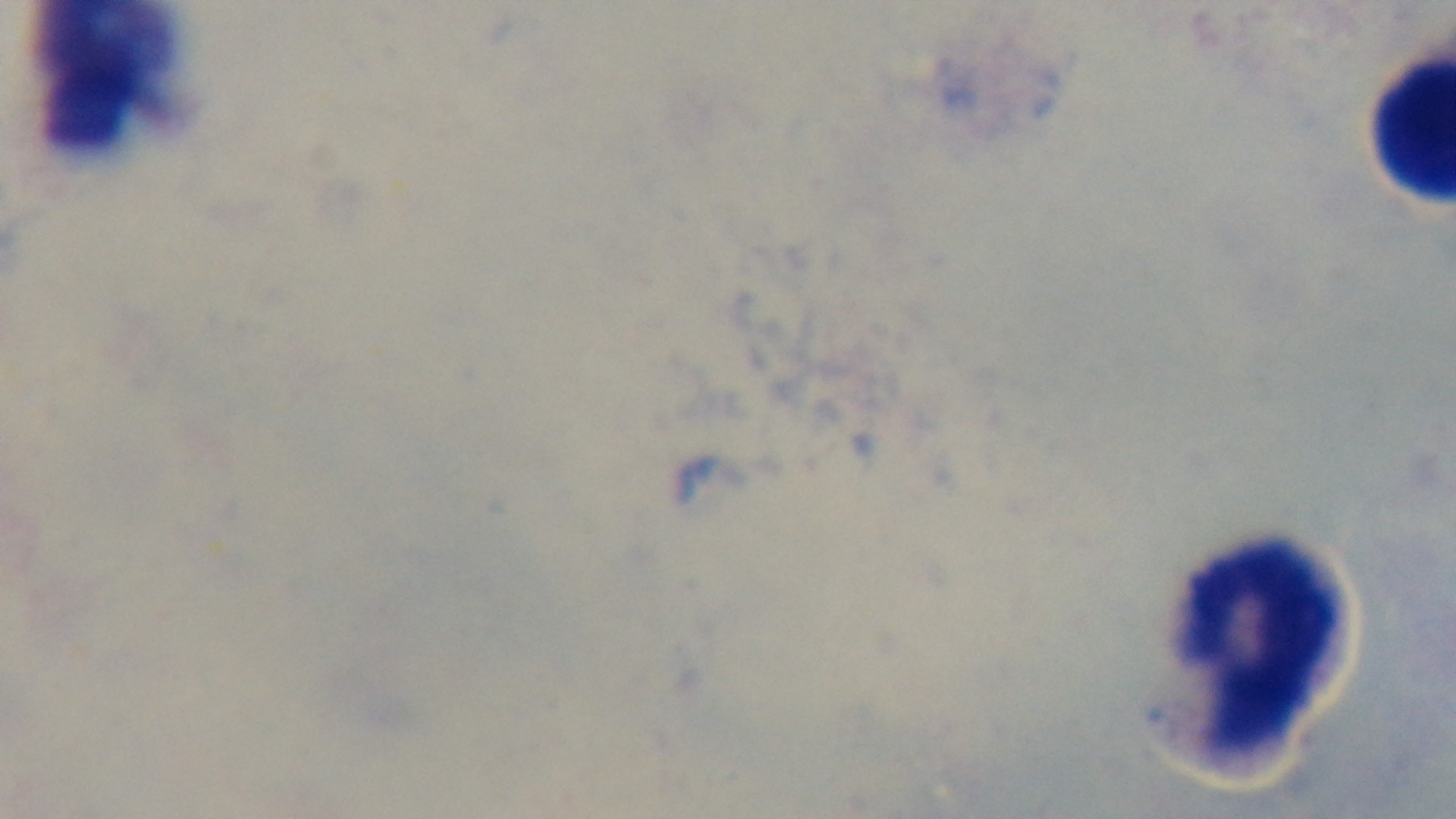
malaria status = negative
modality = light microscopy
objective = 100x oil immersion
capture = mounted 4K digital camera
stain = Giemsa
preparation = thick smear
field of view = single